Assess this cell for malaria.
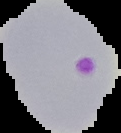

It is parasitized.

image type = segmented cell region on a black background
preparation = thin blood film
image size = 121×133 pixels